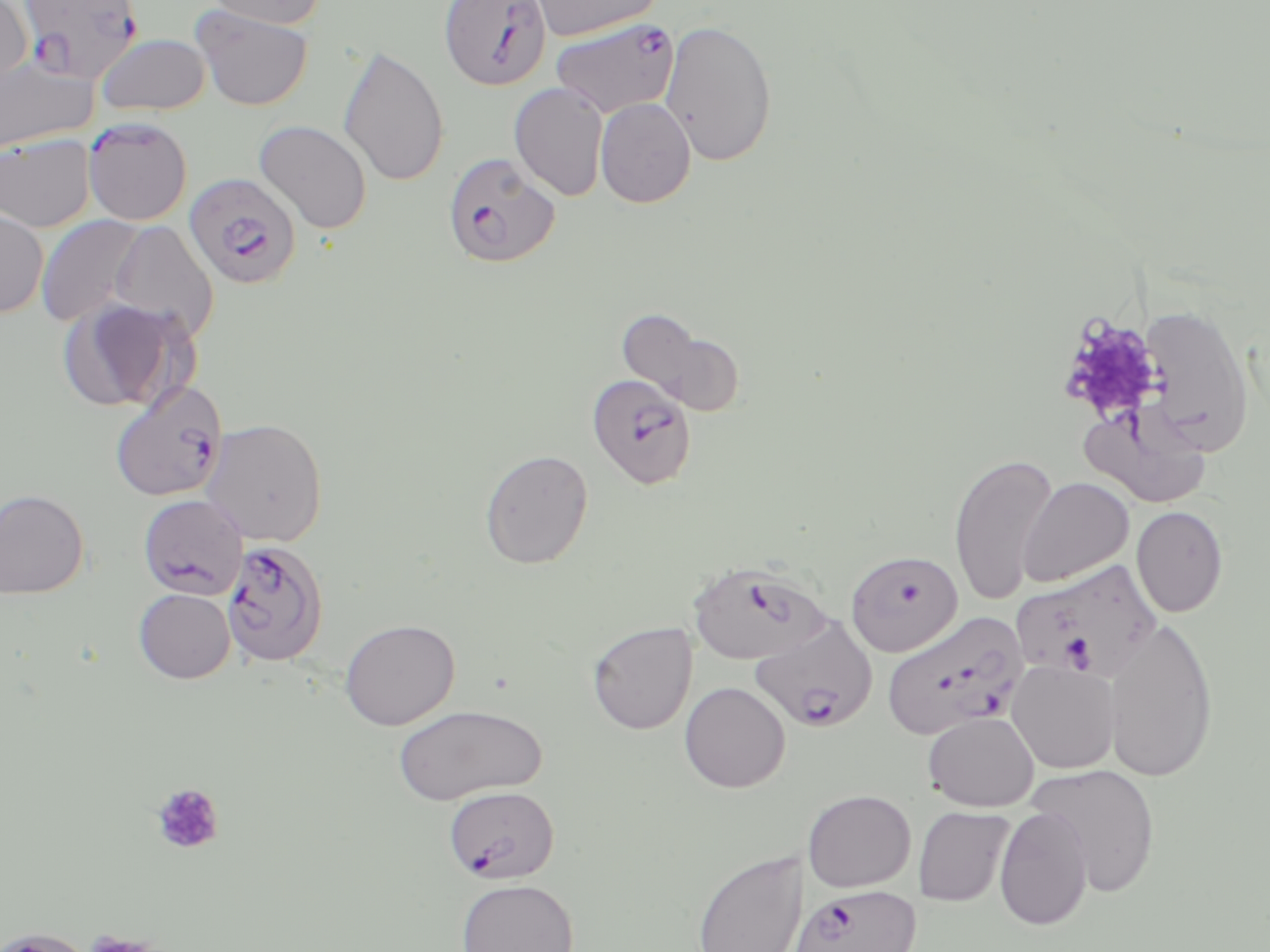

slide-level diagnosis = Plasmodium falciparum
magnification = 1000x
Plasmodium falciparum-infected red blood cell locations (subset) = approximate bounding boxes as [x1, y1, x2, y2] in pixels: [18, 0, 144, 84], [439, 0, 552, 91], [550, 18, 680, 118], [83, 118, 192, 225], [443, 152, 560, 268], [184, 172, 302, 291], [109, 379, 229, 502], [138, 494, 249, 599], [228, 544, 325, 666], [687, 561, 828, 665], [1012, 561, 1161, 681], [881, 610, 1029, 741], [750, 615, 877, 734], [443, 785, 559, 884], [786, 884, 921, 952]
field of view = one of a larger specimen
image size = 1270×952 pixels
platelet locations = approximate bounding boxes as [x1, y1, x2, y2] in pixels: [1057, 312, 1165, 423], [151, 783, 225, 855], [81, 931, 162, 952]
modality = optical microscopy
uninfected red blood cell locations (subset) = approximate bounding boxes as [x1, y1, x2, y2] in pixels: [202, 0, 327, 29], [528, 0, 664, 41], [0, 1, 33, 89], [192, 4, 314, 111], [660, 19, 778, 167], [96, 33, 212, 117], [337, 44, 449, 188], [0, 57, 97, 155], [509, 82, 609, 201], [595, 98, 696, 208], [254, 120, 372, 234], [0, 133, 96, 232], [0, 208, 49, 318], [34, 214, 149, 329], [108, 220, 219, 343], [56, 298, 195, 414], [1139, 304, 1255, 456], [617, 310, 745, 418], [1082, 404, 1211, 507], [200, 417, 328, 548], [479, 449, 593, 569], [948, 451, 1058, 605], [1017, 477, 1134, 587], [0, 488, 88, 599], [1131, 506, 1228, 617], [846, 550, 963, 656], [133, 588, 235, 683], [339, 618, 460, 730], [1103, 618, 1219, 783], [587, 622, 697, 735], [1007, 660, 1120, 774], [679, 681, 791, 793], [393, 704, 546, 805], [923, 711, 1039, 811], [1026, 763, 1160, 897], [803, 789, 915, 892], [913, 806, 1015, 907], [994, 807, 1094, 930], [690, 847, 807, 952], [456, 878, 579, 952], [0, 928, 96, 952]
stain = May-Grünwald-Giemsa
preparation = thin blood smear